Locate every Plasmodium parasite.
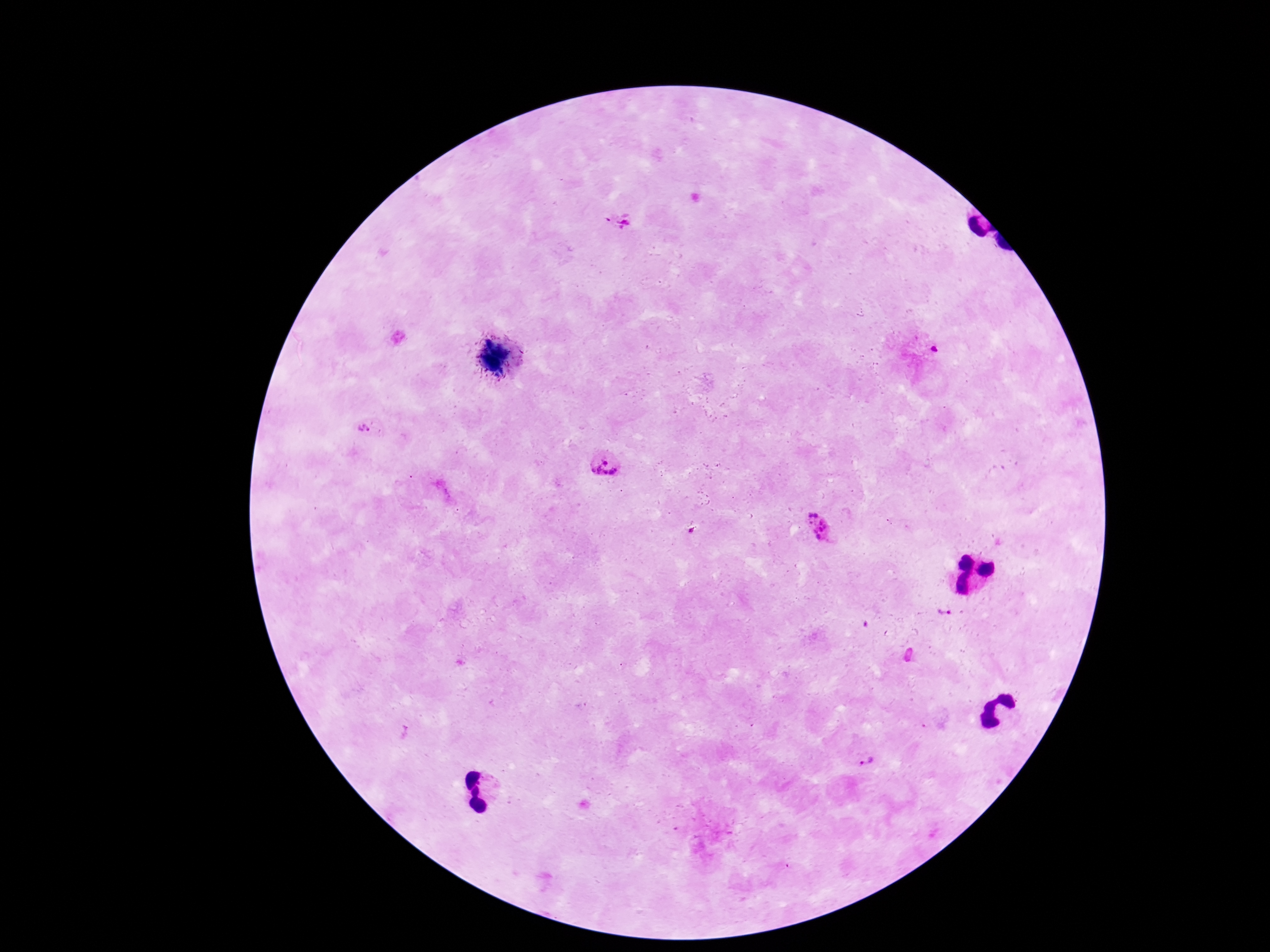

Approximate centers as {x, y} in pixels.
Plasmodium parasites: {619, 221}, {932, 348}, {370, 429}, {606, 465}, {822, 528}, {944, 613}, {862, 761}.

Image is 1270×952 pixels. One field from this slide. Smartphone photograph taken through the microscope eyepiece. Giemsa-stained preparation. Thick blood film. Patient malaria status: infected. 100x magnification.